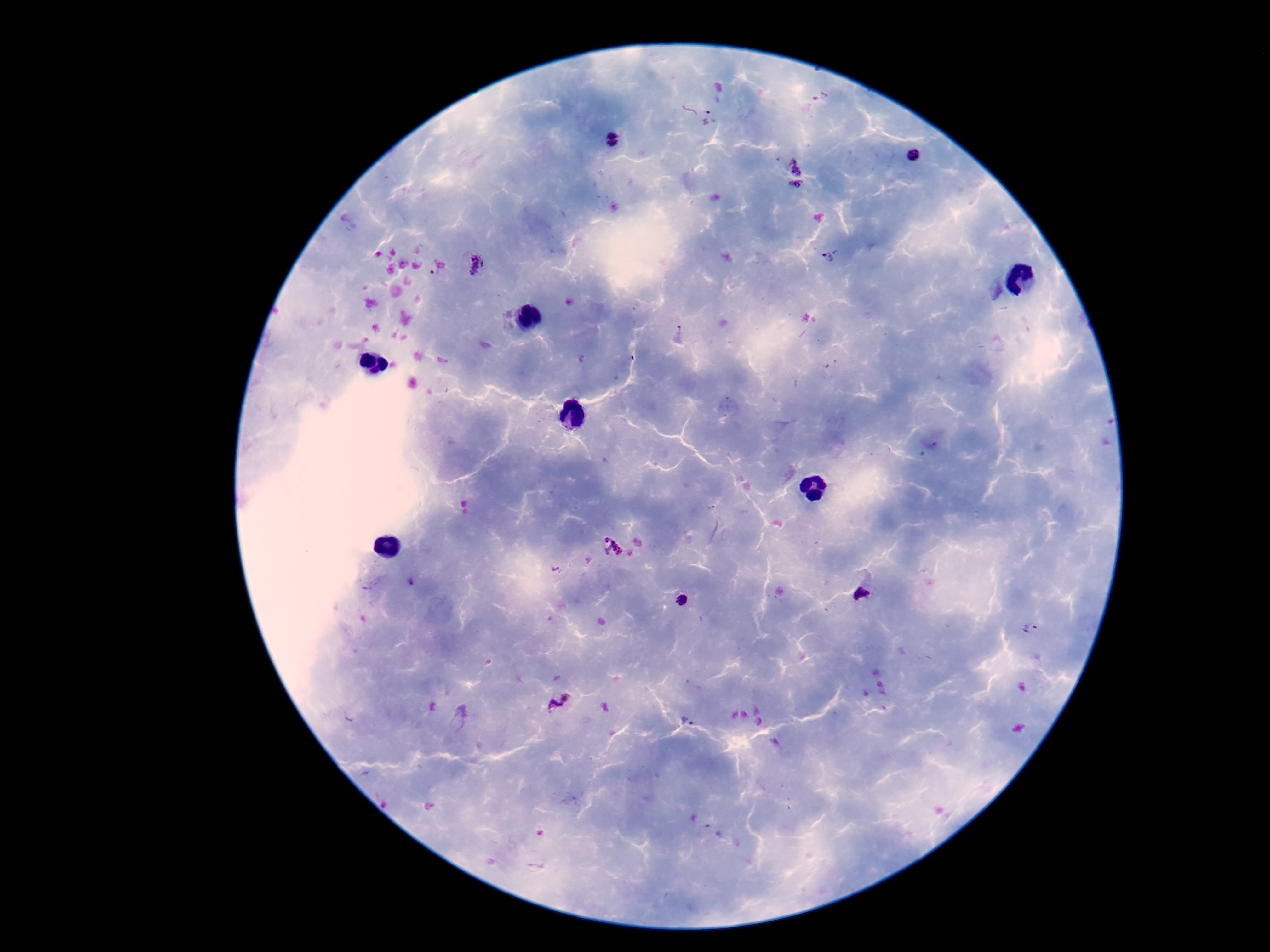

Approximate centers as {x, y} in pixels.
Summary:
  - Plasmodium parasite locations: {697, 114}, {611, 141}, {912, 155}, {798, 166}, {796, 187}, {828, 258}, {476, 265}, {432, 269}, {616, 549}, {554, 569}, {862, 594}, {680, 596}, {1030, 630}, {558, 702}, {686, 721}
  - Magnification: 100x
  - Patient malaria status: positive
  - Image size: 1270×952 pixels
  - Field of view: single
  - Preparation: thick blood film
  - Stain: Giemsa
  - Capture: smartphone camera through the microscope eyepiece